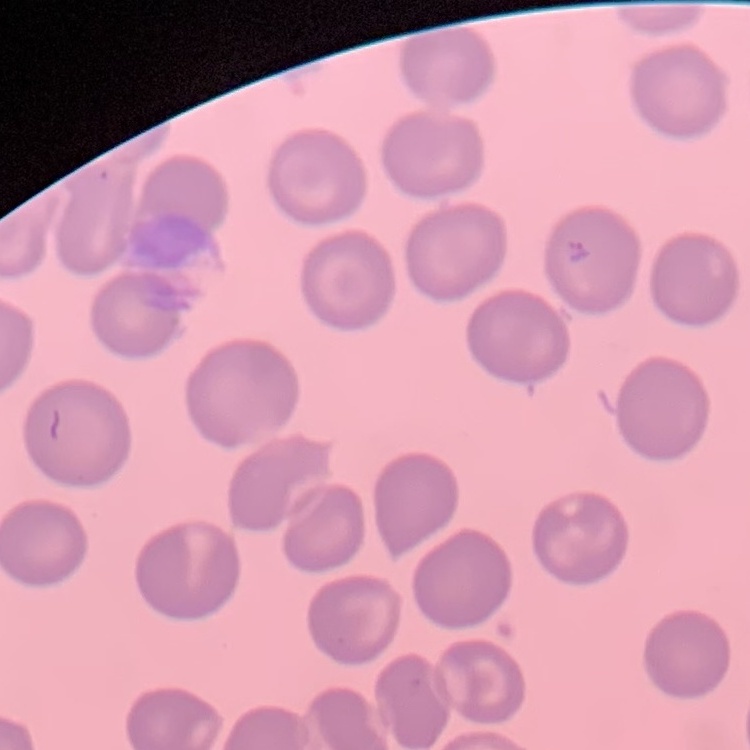
Summary:
  - Erythrocyte morphology: no rouleaux formation
  - Preparation: thin blood film
  - Image type: one tile cut from a larger photomicrograph
  - Stain: Field's or Giemsa